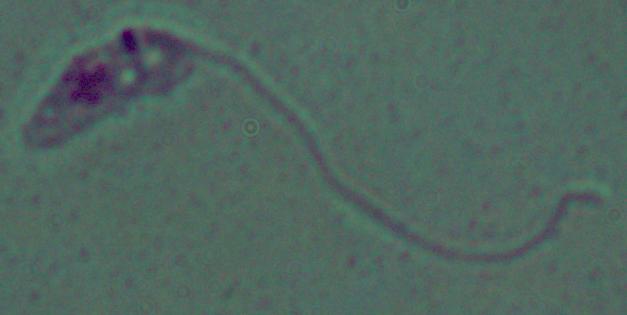
magnification: 1000x
identification: Leishmania
modality: photomicrograph